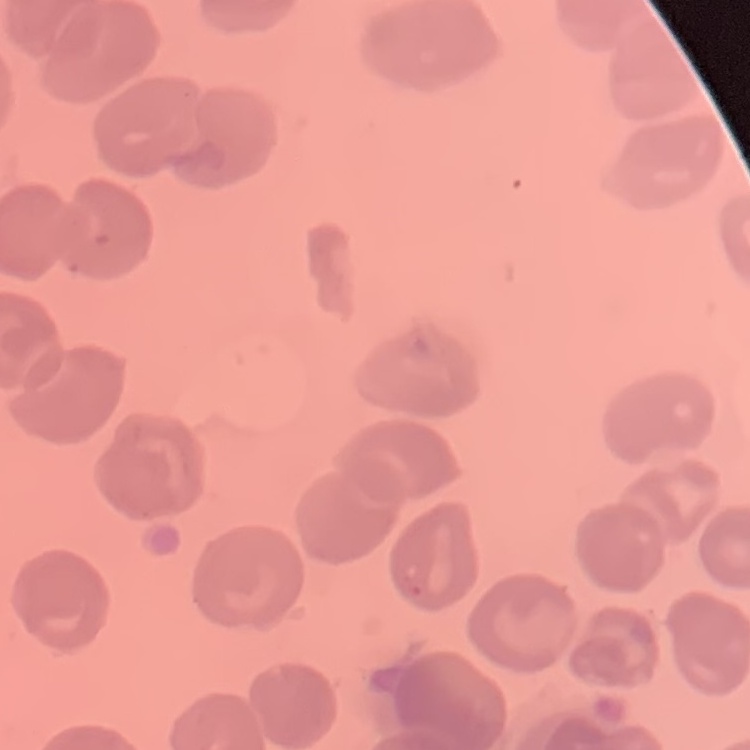
Summary:
  - Erythrocyte morphology: no rouleaux formation
  - Image type: square crop of a larger photomicrograph
  - Preparation: thin peripheral smear
  - Stain: Field's or Giemsa